Evaluate for malaria.
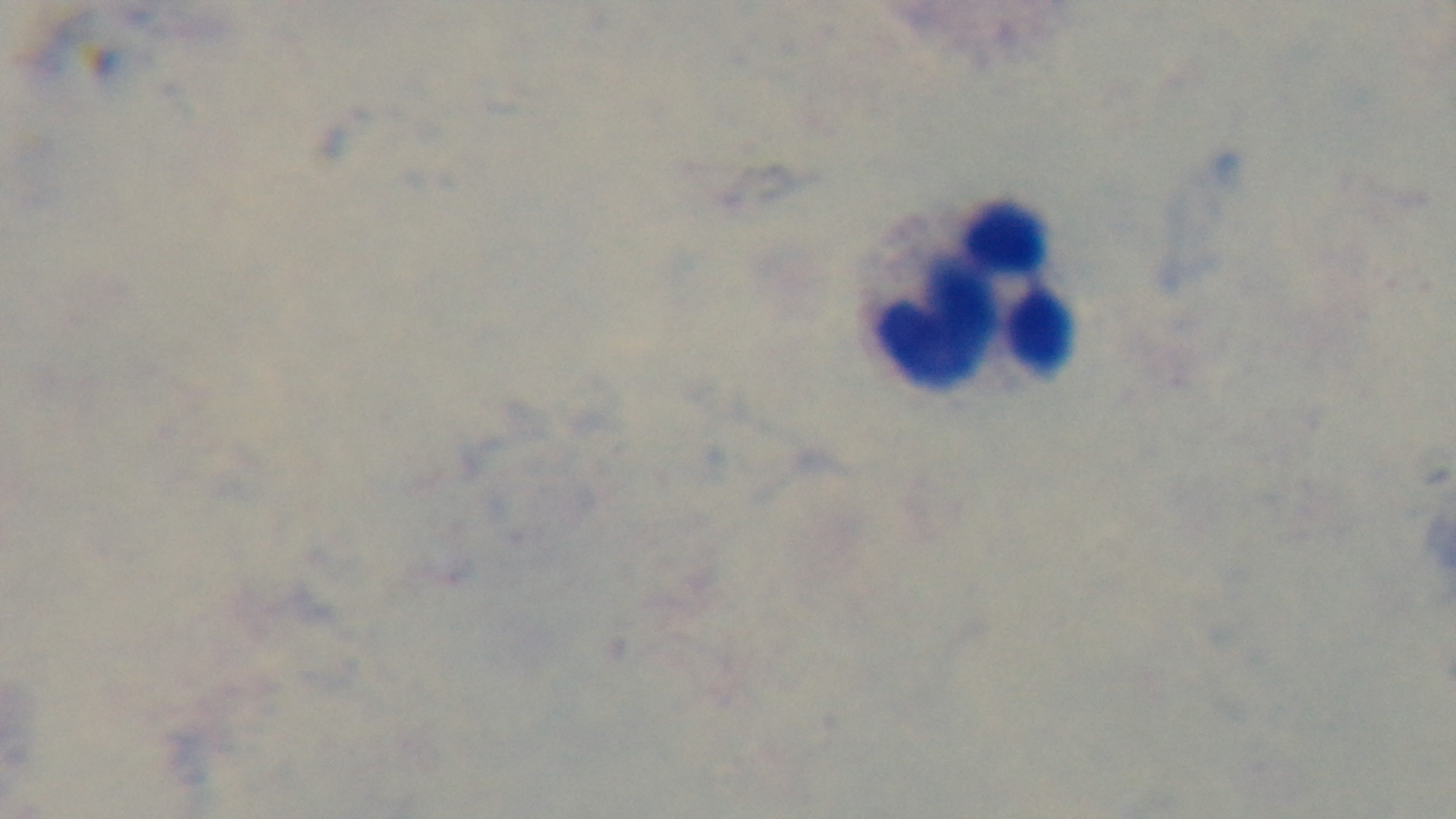

Negative.

Summary:
  - Capture: mounted 4K digital camera
  - Stain: Giemsa
  - Objective: 100x oil immersion
  - Preparation: thick blood film
  - Modality: light microscopy
  - Field of view: single